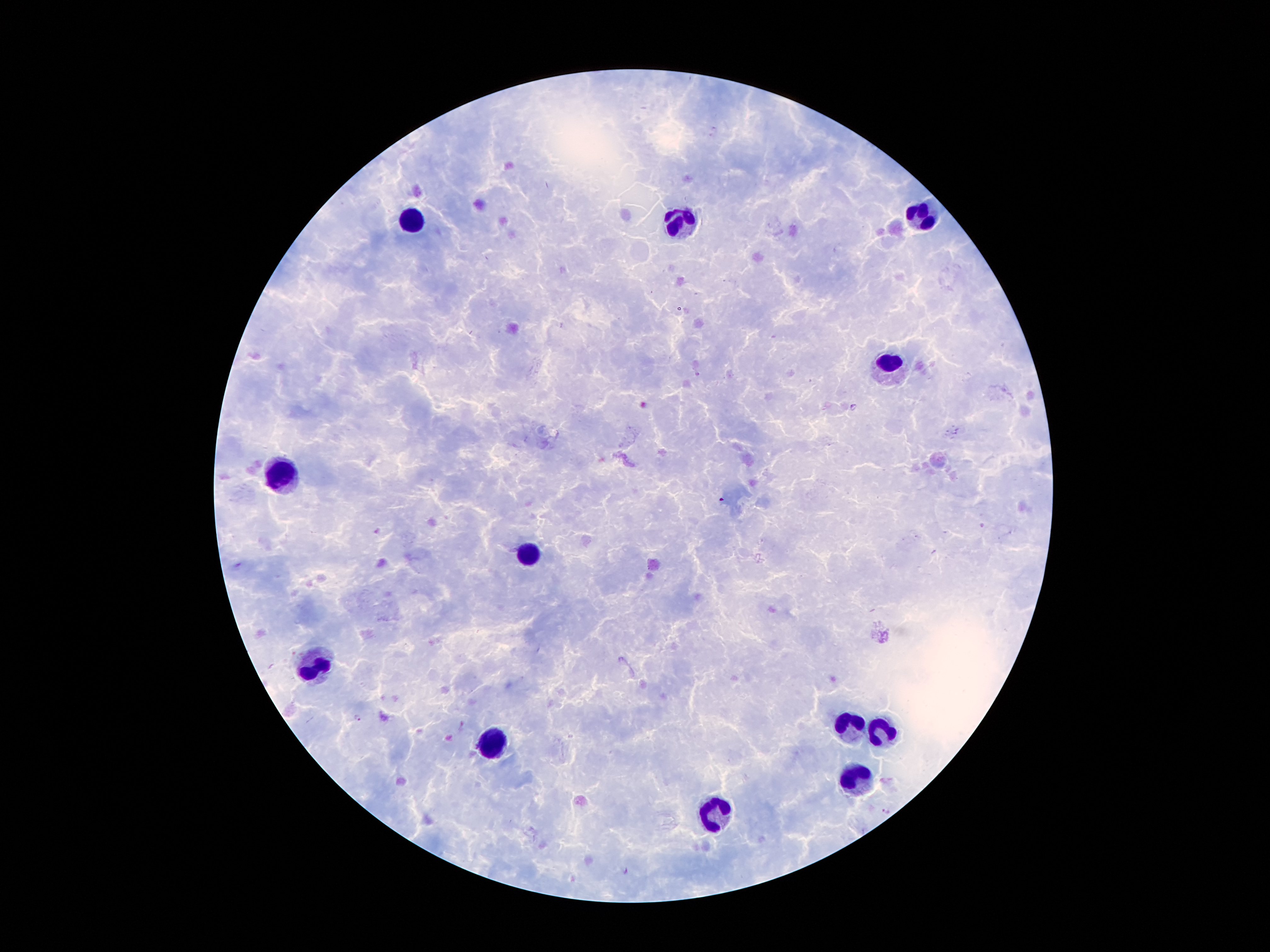

plasmodium_parasite_locations: 'approximate centers as [x, y] in pixels: [856, 407], [356, 716], [886, 810], [624, 869]'
capture: smartphone camera through the microscope eyepiece
preparation: thick peripheral-blood smear
leukocyte_locations: 'approximate centers as [x, y] in pixels: [919, 209], [413, 219], [682, 219], [890, 365], [279, 476], [526, 550], [316, 664], [848, 725], [877, 730], [494, 745], [853, 775], [712, 812]'
patient_malaria_status: infected with Plasmodium falciparum
magnification: 100x
image_size: 1270×952 pixels
field_of_view: one from this slide
stain: Giemsa